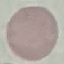 Result: no malaria parasites seen. Thin blood smear. Giemsa-stained preparation. Acquired by smartphone through the microscope eyepiece. Automatically extracted cell patch, resized to 64 × 64 pixels.